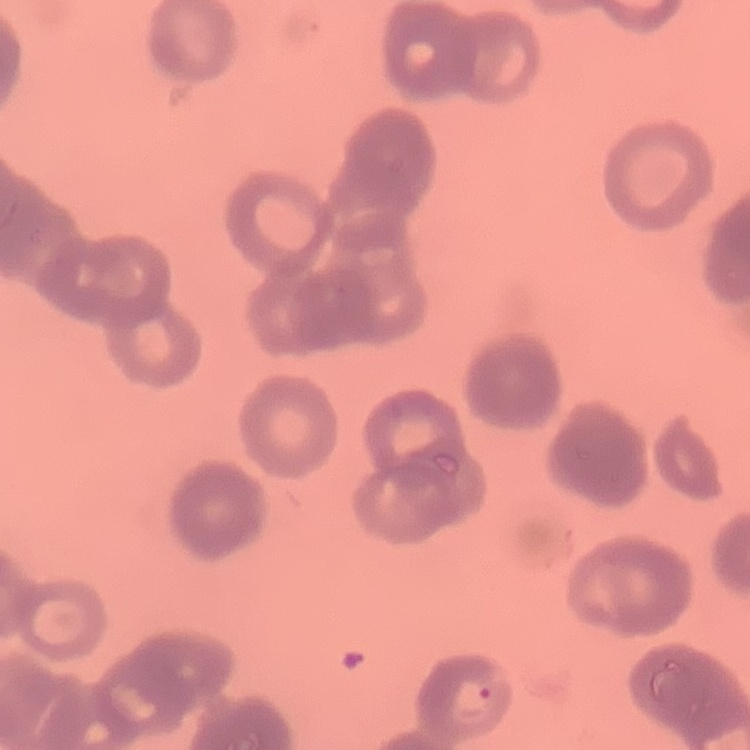

Summary:
  - Red blood cell morphology: rouleaux formation
  - Stain: Field's or Giemsa
  - Image type: square crop of a larger photomicrograph
  - Preparation: thin blood film